Classify this cell by malaria status.
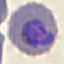

Parasitized.

Photographed with a smartphone camera at the microscope eyepiece. Automatically extracted cell patch, resized to 64 × 64 pixels. Giemsa stain. Thin blood smear.